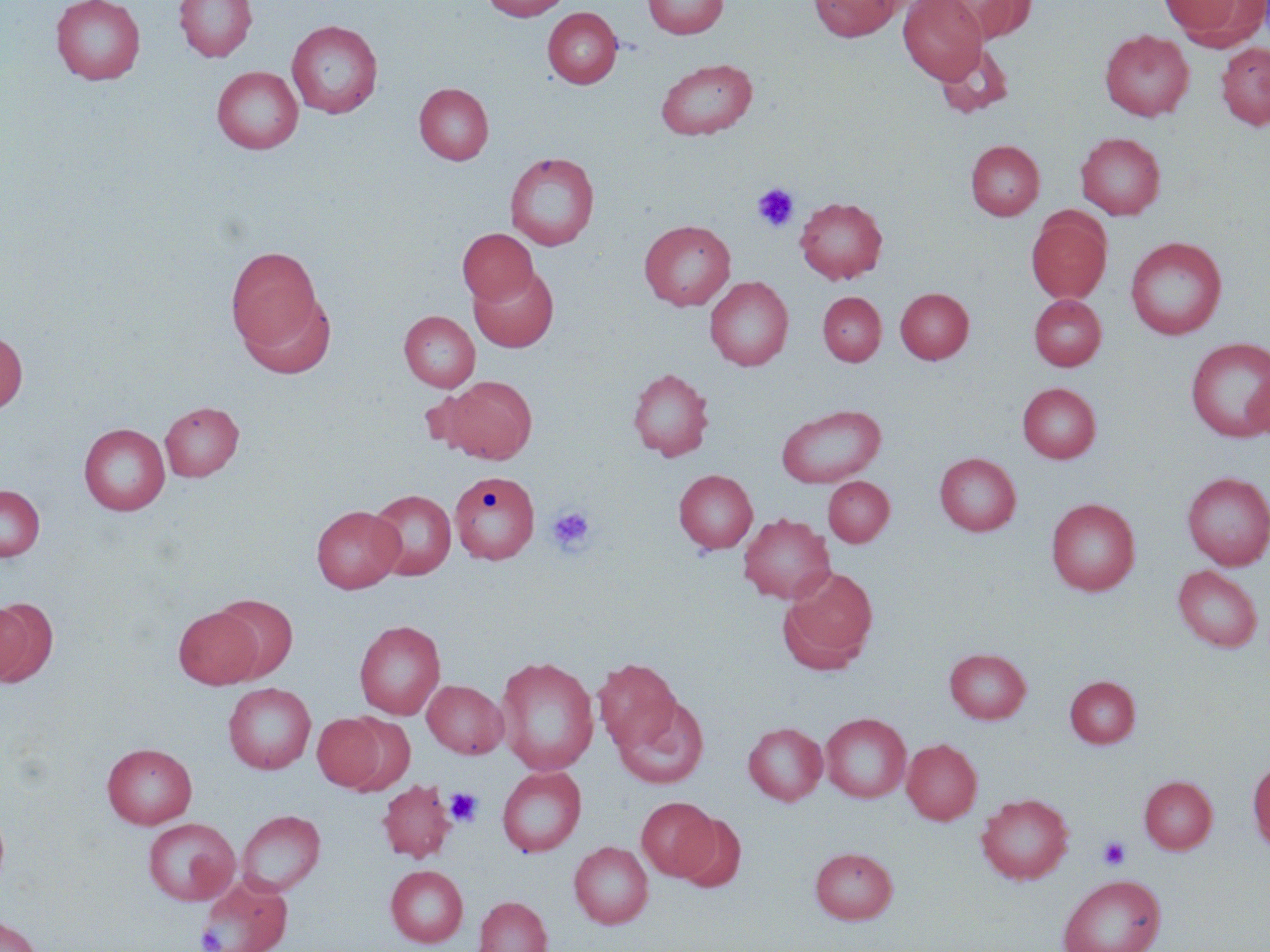

Summary:
  - Coordinate format: approximate bounding boxes as [x1, y1, x2, y2] in pixels
  - Platelet locations: [752, 183, 799, 232], [546, 505, 596, 555], [444, 787, 483, 827], [1098, 837, 1131, 870], [197, 926, 226, 951]
  - Uninfected red blood cell locations: [51, 0, 146, 85], [174, 0, 256, 62], [482, 0, 570, 21], [642, 0, 729, 39], [808, 0, 900, 41], [898, 0, 987, 83], [1159, 0, 1258, 41], [936, 1, 1037, 45], [543, 7, 622, 88], [286, 20, 383, 118], [1100, 30, 1194, 121], [1216, 42, 1270, 130], [935, 44, 1015, 117], [655, 58, 758, 140], [212, 66, 303, 154], [414, 82, 494, 165], [1076, 132, 1165, 219], [965, 140, 1044, 220], [504, 151, 600, 250], [795, 196, 887, 283], [1026, 210, 1111, 302], [639, 220, 736, 310], [456, 228, 539, 306], [1125, 236, 1227, 339], [226, 245, 325, 355], [468, 265, 559, 352], [705, 276, 793, 371], [895, 287, 973, 363], [238, 290, 337, 380], [817, 291, 886, 366], [1029, 295, 1106, 370], [399, 310, 480, 392], [0, 331, 28, 414], [1185, 337, 1270, 443], [628, 367, 714, 461], [441, 376, 538, 463], [1018, 382, 1100, 463], [160, 401, 243, 481], [776, 404, 886, 487], [79, 423, 170, 515], [935, 452, 1021, 535], [674, 469, 757, 554], [450, 471, 539, 565], [1182, 472, 1270, 570], [823, 476, 893, 546], [0, 485, 45, 561], [367, 489, 457, 580], [1046, 498, 1140, 595], [311, 505, 404, 593], [738, 513, 835, 604], [1173, 565, 1263, 652], [780, 566, 878, 670], [211, 594, 297, 681], [0, 598, 54, 687], [174, 606, 263, 689], [354, 620, 445, 720], [945, 648, 1031, 723], [495, 655, 599, 775], [594, 659, 681, 751], [1065, 676, 1140, 748], [422, 680, 508, 758], [223, 683, 316, 774], [614, 696, 710, 789], [312, 713, 386, 790], [338, 713, 415, 794], [822, 713, 910, 802], [743, 722, 827, 805], [902, 738, 982, 825], [102, 743, 197, 828], [1248, 760, 1270, 853], [497, 766, 586, 857], [1140, 776, 1217, 854], [377, 780, 456, 862], [976, 793, 1074, 884], [636, 796, 718, 879], [236, 809, 325, 896], [674, 814, 747, 893], [142, 817, 240, 905], [569, 840, 653, 929], [810, 847, 898, 924], [385, 865, 468, 947], [196, 874, 293, 952], [1057, 874, 1166, 952], [474, 896, 552, 952], [0, 915, 43, 952]
  - Slide-level diagnosis: no evidence of blood parasites
  - Modality: light microscopy
  - Magnification: 1000x
  - Field of view: one of a larger specimen
  - Image size: 1270×952 pixels
  - Preparation: thin blood smear
  - Stain: May-Grünwald-Giemsa